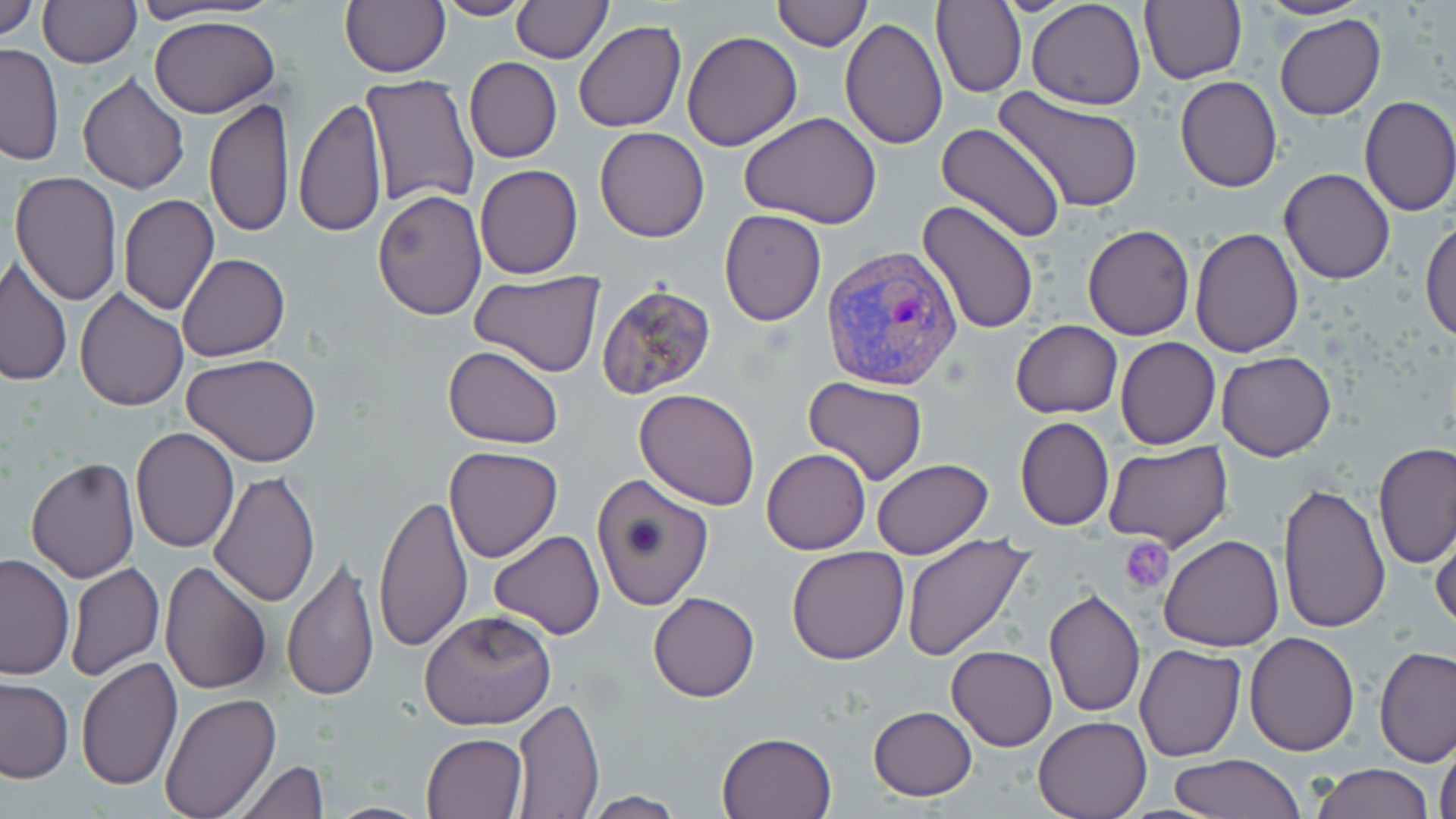
plasmodium_vivax_infected_red_blood_cell_locations: 'approximate bounding boxes as [x1, y1, x2, y2] in pixels: [821, 246, 963, 393]'
slide_level_diagnosis: Plasmodium vivax
stain: May-Grünwald-Giemsa
field_of_view: one of a larger specimen
image_size: 1456×819 pixels
uninfected_red_blood_cell_locations: 'approximate bounding boxes as [x1, y1, x2, y2] in pixels: [0, 0, 40, 44], [38, 0, 140, 68], [340, 0, 449, 78], [434, 0, 533, 21], [512, 0, 610, 62], [770, 0, 870, 51], [931, 0, 1026, 98], [1026, 0, 1147, 111], [1140, 0, 1248, 86], [1256, 0, 1371, 20], [149, 14, 281, 119], [1275, 15, 1386, 121], [841, 17, 947, 150], [572, 22, 686, 132], [682, 31, 801, 149], [0, 43, 65, 166], [464, 57, 562, 163], [76, 73, 191, 193], [360, 75, 482, 211], [1175, 75, 1283, 192], [997, 87, 1142, 213], [1358, 95, 1456, 217], [294, 98, 388, 238], [205, 99, 295, 236], [739, 111, 883, 227], [937, 122, 1067, 245], [593, 127, 710, 243], [474, 163, 583, 279], [1279, 168, 1395, 284], [10, 170, 122, 304], [371, 188, 489, 322], [119, 193, 220, 315], [915, 199, 1039, 336], [719, 209, 826, 327], [1421, 217, 1455, 345], [1082, 224, 1195, 340], [1189, 227, 1303, 357], [177, 253, 289, 361], [2, 258, 73, 386], [469, 272, 605, 378], [595, 283, 718, 400], [75, 287, 189, 411], [1010, 320, 1123, 417], [1115, 337, 1220, 450], [442, 345, 565, 450], [1216, 351, 1337, 461], [182, 354, 321, 465], [803, 377, 929, 486], [634, 388, 762, 512], [1015, 416, 1114, 532], [131, 426, 239, 553], [1104, 440, 1234, 552], [1374, 443, 1456, 569], [443, 446, 563, 563], [761, 448, 871, 555], [25, 459, 140, 583], [871, 459, 995, 560], [208, 471, 320, 609], [591, 474, 715, 613], [1277, 483, 1391, 634], [374, 494, 474, 653], [1430, 519, 1456, 636], [488, 530, 604, 640], [899, 534, 1036, 662], [1160, 535, 1285, 651], [786, 545, 909, 664], [0, 552, 76, 679], [282, 553, 380, 702], [158, 559, 273, 695], [66, 563, 164, 681], [1044, 587, 1147, 719], [648, 592, 759, 703], [418, 608, 557, 730], [1244, 631, 1360, 756], [1135, 644, 1247, 763], [947, 646, 1057, 751], [1374, 646, 1456, 766], [76, 657, 184, 793], [0, 678, 73, 782], [158, 692, 282, 819], [511, 697, 604, 815], [867, 705, 978, 800], [1032, 716, 1151, 819], [716, 731, 837, 819], [422, 732, 527, 817], [1434, 741, 1456, 819], [1169, 753, 1306, 819], [233, 759, 329, 818], [1310, 764, 1435, 819], [583, 792, 688, 818]'
platelet_locations: 'approximate bounding boxes as [x1, y1, x2, y2] in pixels: [1119, 536, 1175, 595]'
modality: light microscopy
preparation: thin blood film
magnification: 1000x